Name the parasite shown.
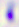

Toxoplasma gondii.

Captured at 400x magnification. Micrograph.